Report the malaria status of this cell.
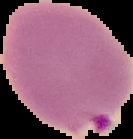

Parasitized.

Summary:
  - Preparation: thin blood smear
  - Image size: 133×139 pixels
  - Image type: segmented cell region on a black background